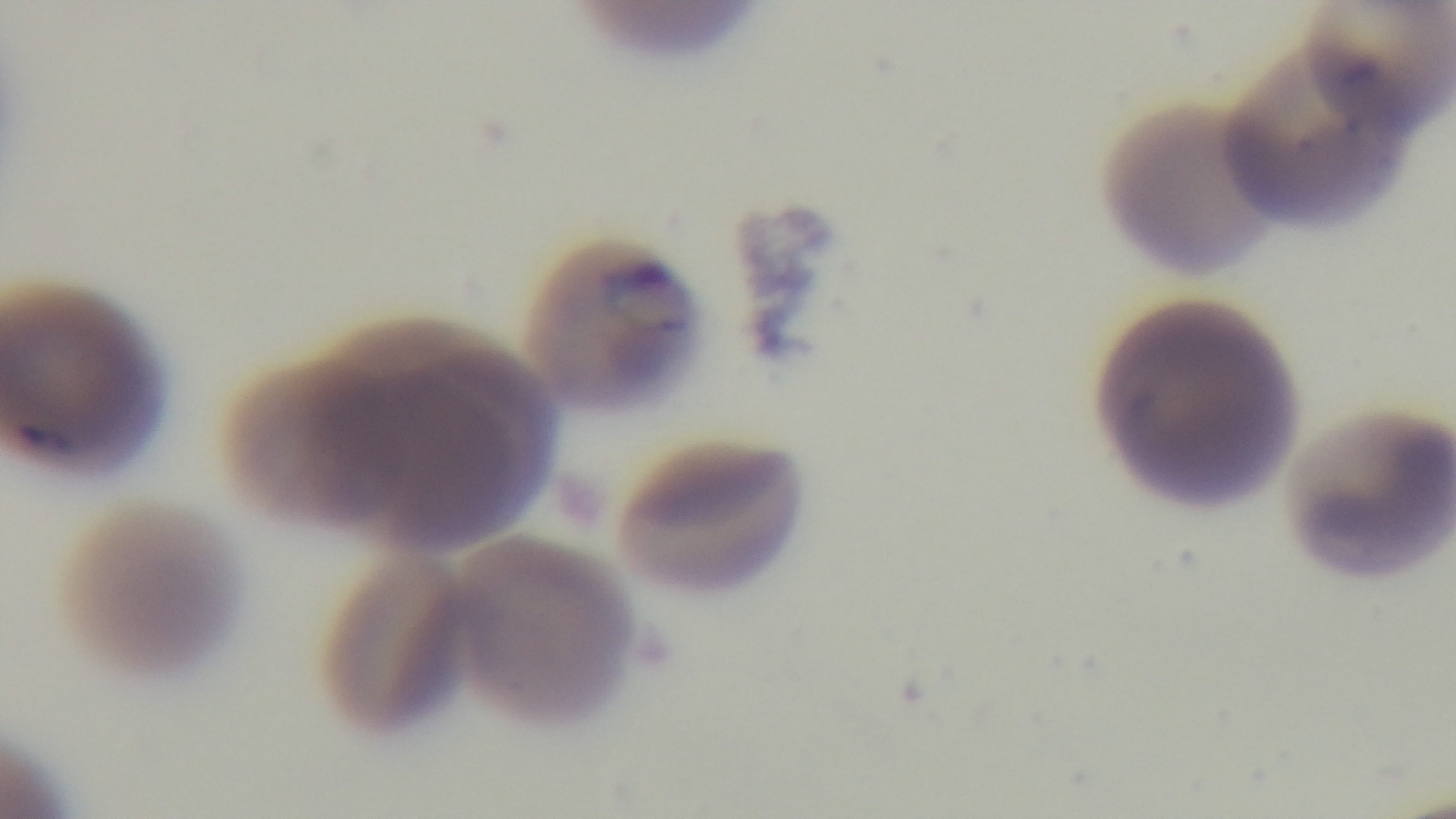
Summary:
  - Malaria status: infected
  - Capture: mounted 4K digital camera
  - Preparation: thin
  - Stain: Giemsa
  - Objective: 100x oil immersion
  - Field of view: single
  - Modality: light microscopy